Outline each uninfected red blood cell.
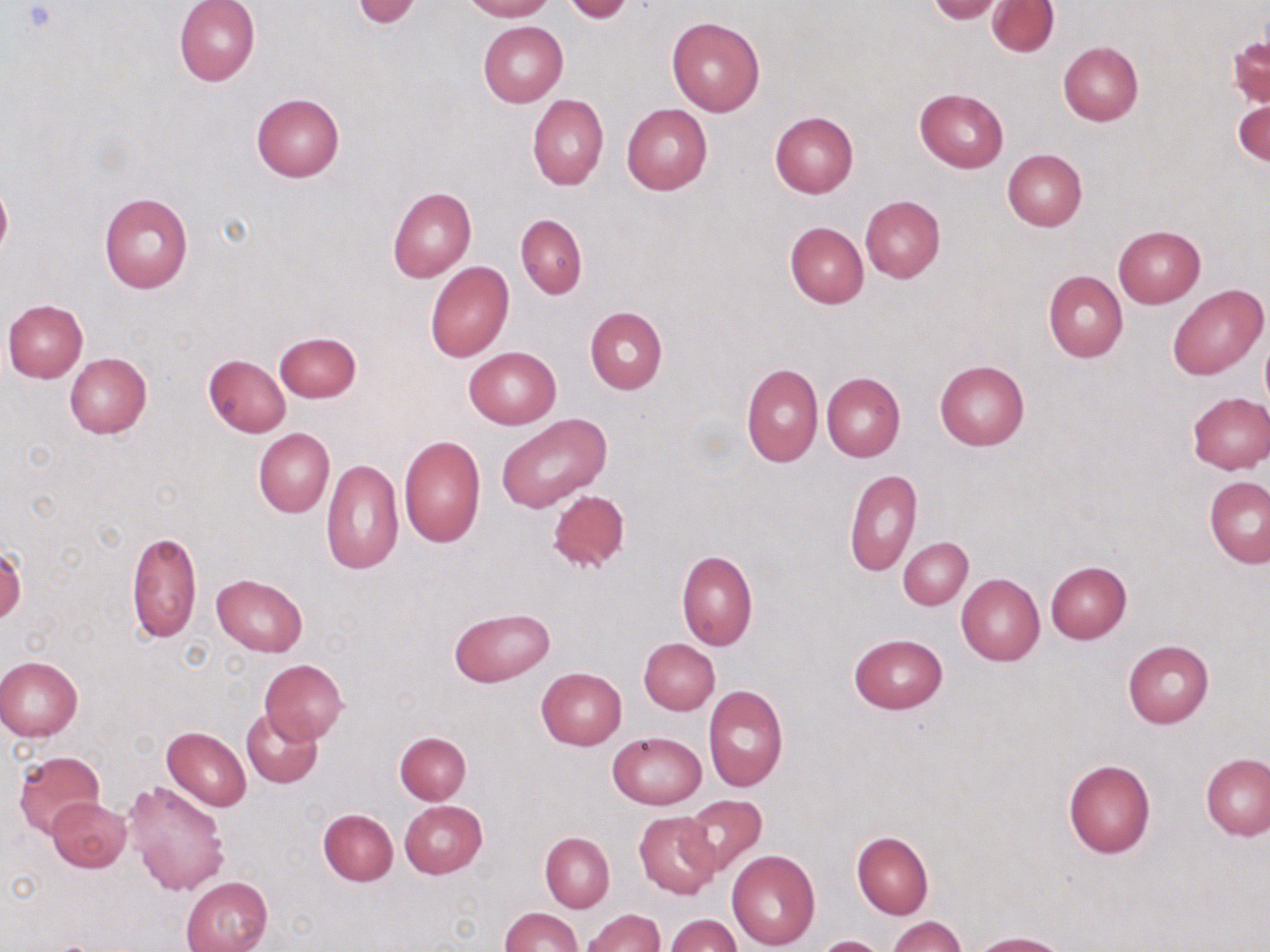

Approximate bounding boxes as [x1, y1, x2, y2] in pixels.
Uninfected red blood cells: [175, 0, 259, 86], [463, 0, 552, 21], [352, 1, 422, 28], [563, 1, 634, 23], [928, 1, 1002, 23], [988, 1, 1058, 56], [667, 16, 765, 117], [478, 21, 568, 106], [1058, 41, 1143, 126], [914, 88, 1009, 172], [252, 94, 344, 182], [527, 94, 608, 190], [1234, 95, 1269, 168], [622, 103, 712, 194], [769, 111, 858, 198], [1003, 149, 1086, 231], [0, 184, 12, 258], [387, 186, 476, 283], [98, 193, 193, 293], [860, 195, 945, 282], [515, 214, 588, 298], [785, 222, 869, 308], [1114, 225, 1206, 308], [425, 262, 513, 362], [1043, 270, 1127, 362], [1166, 284, 1268, 380], [3, 300, 87, 383], [585, 307, 667, 395], [275, 331, 361, 403], [1260, 333, 1270, 409], [464, 346, 561, 429], [64, 353, 152, 438], [203, 354, 291, 437], [934, 361, 1029, 450], [741, 363, 823, 468], [822, 371, 905, 462], [1186, 391, 1270, 474], [496, 414, 610, 514], [253, 428, 334, 517], [398, 435, 486, 548], [319, 458, 402, 574], [845, 468, 922, 577], [1204, 475, 1270, 567], [547, 489, 631, 572], [127, 530, 201, 644], [898, 537, 972, 610], [1, 545, 25, 623], [677, 550, 757, 650], [1045, 561, 1132, 643], [212, 573, 308, 656], [957, 573, 1044, 665], [448, 606, 555, 686], [849, 632, 948, 714], [639, 639, 720, 715], [1123, 640, 1214, 728], [0, 656, 82, 740], [260, 659, 348, 743], [536, 667, 627, 749], [703, 685, 788, 791], [241, 707, 322, 788], [162, 727, 252, 811], [394, 731, 472, 804], [608, 731, 706, 809], [13, 751, 105, 837], [1202, 753, 1269, 840], [1063, 759, 1155, 858], [123, 780, 229, 896], [681, 795, 768, 876], [48, 796, 131, 872], [399, 800, 487, 878], [318, 808, 398, 885], [634, 812, 721, 899], [852, 831, 933, 919], [541, 832, 615, 912], [727, 850, 820, 950], [182, 876, 272, 952], [501, 907, 579, 952], [584, 909, 664, 952], [665, 915, 741, 952], [888, 916, 964, 952], [973, 932, 1067, 952], [814, 935, 889, 952].

slide_level_diagnosis: negative for blood parasites
field_of_view: one of a larger specimen
preparation: thin blood smear
stain: May-Grünwald-Giemsa
image_size: 1270×952 pixels
magnification: 1000x
modality: light microscopy